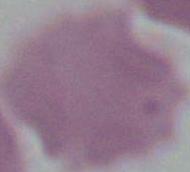

An erythrocyte is seen. 1000x magnification. Photomicrograph.